State which parasite is depicted.
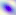
Toxoplasma gondii.

magnification = 400x
modality = micrograph